Assess this cell for malaria.
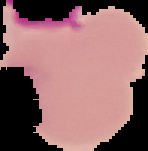
Uninfected.

Summary:
  - Image size: 148×151 pixels
  - Preparation: thin blood film
  - Image type: cell region segmented out of the field of view; surrounding area masked to black